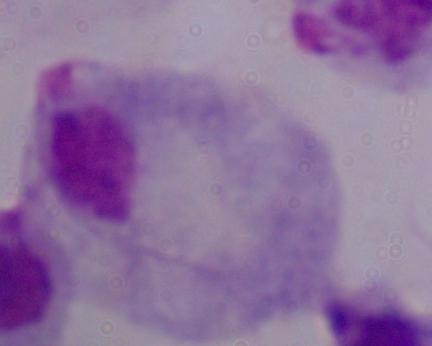

Summary:
  - Modality: micrograph
  - Magnification: 1000x
  - Identification: trichomonad